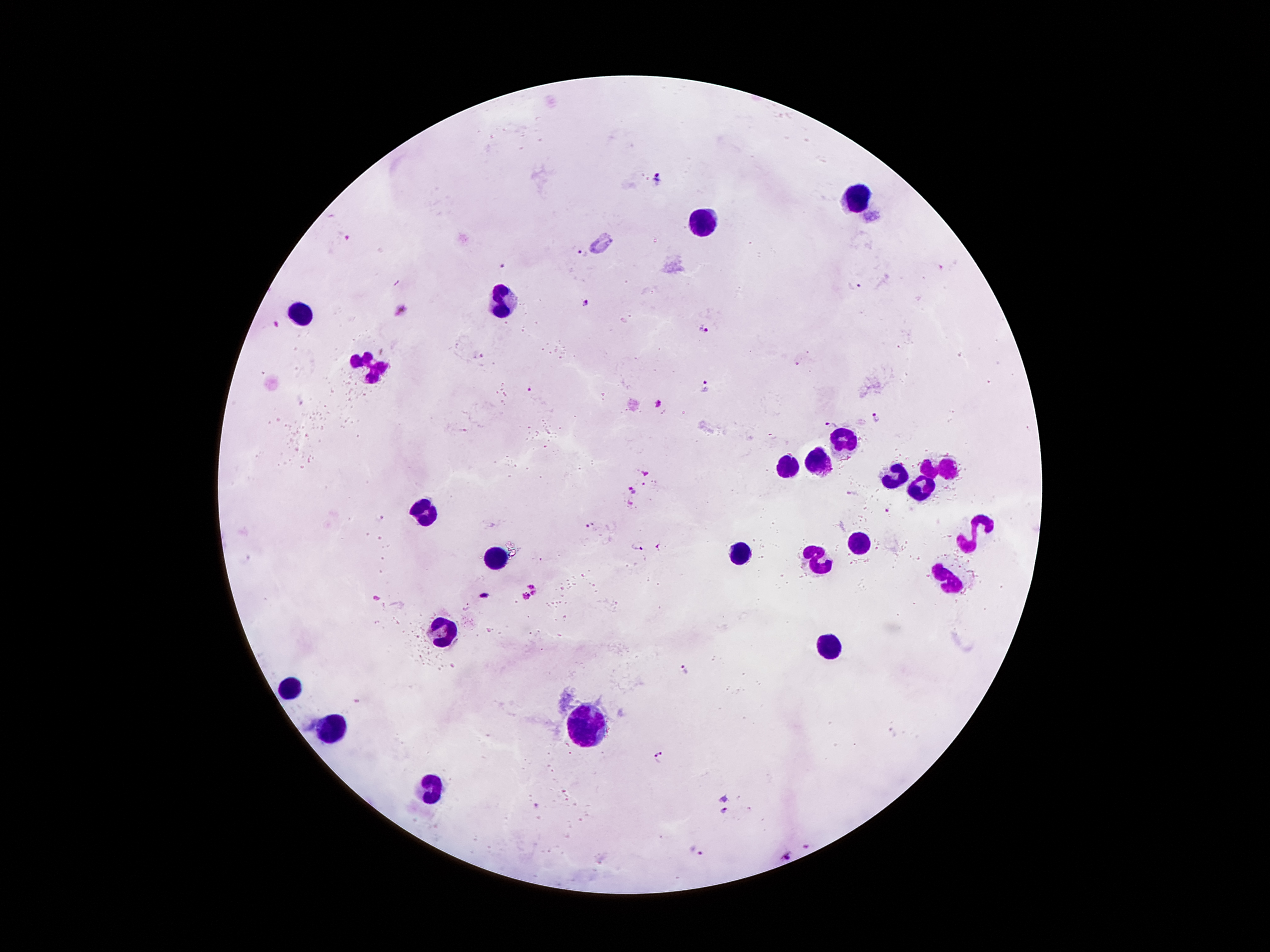 Approximate centers as (x, y) in pixels. Leukocyte locations: (857, 196), (705, 225), (507, 301), (304, 312), (368, 367), (837, 438), (821, 462), (787, 467), (941, 468), (890, 477), (918, 488), (427, 513), (975, 535), (860, 542), (739, 550), (816, 555), (496, 556), (945, 580), (444, 633), (831, 647), (289, 684), (588, 723), (336, 727), (431, 786). Malaria parasite locations: (657, 177), (343, 235), (583, 253), (500, 265), (854, 287), (587, 302), (399, 309), (276, 323), (705, 329), (479, 353), (709, 385), (528, 390), (657, 403), (876, 417), (829, 425), (646, 471), (631, 491), (853, 495), (887, 508), (379, 519), (588, 526), (638, 546), (661, 548), (534, 584), (484, 595), (376, 596), (528, 597), (683, 670), (895, 731), (661, 756), (726, 799), (722, 811), (698, 850), (788, 855). One field from this slide. Image is 1270×952 pixels. Giemsa stain. Photographed through the microscope eyepiece with a smartphone camera. Patient malaria status: positive for Plasmodium falciparum. Thick blood film. 100x magnification.